Identify the parasite.
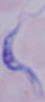

A trypanosome.

Summary:
  - Modality: photomicrograph
  - Magnification: 1000x